Give the extent of all Plasmodium ovale-infected red blood cells.
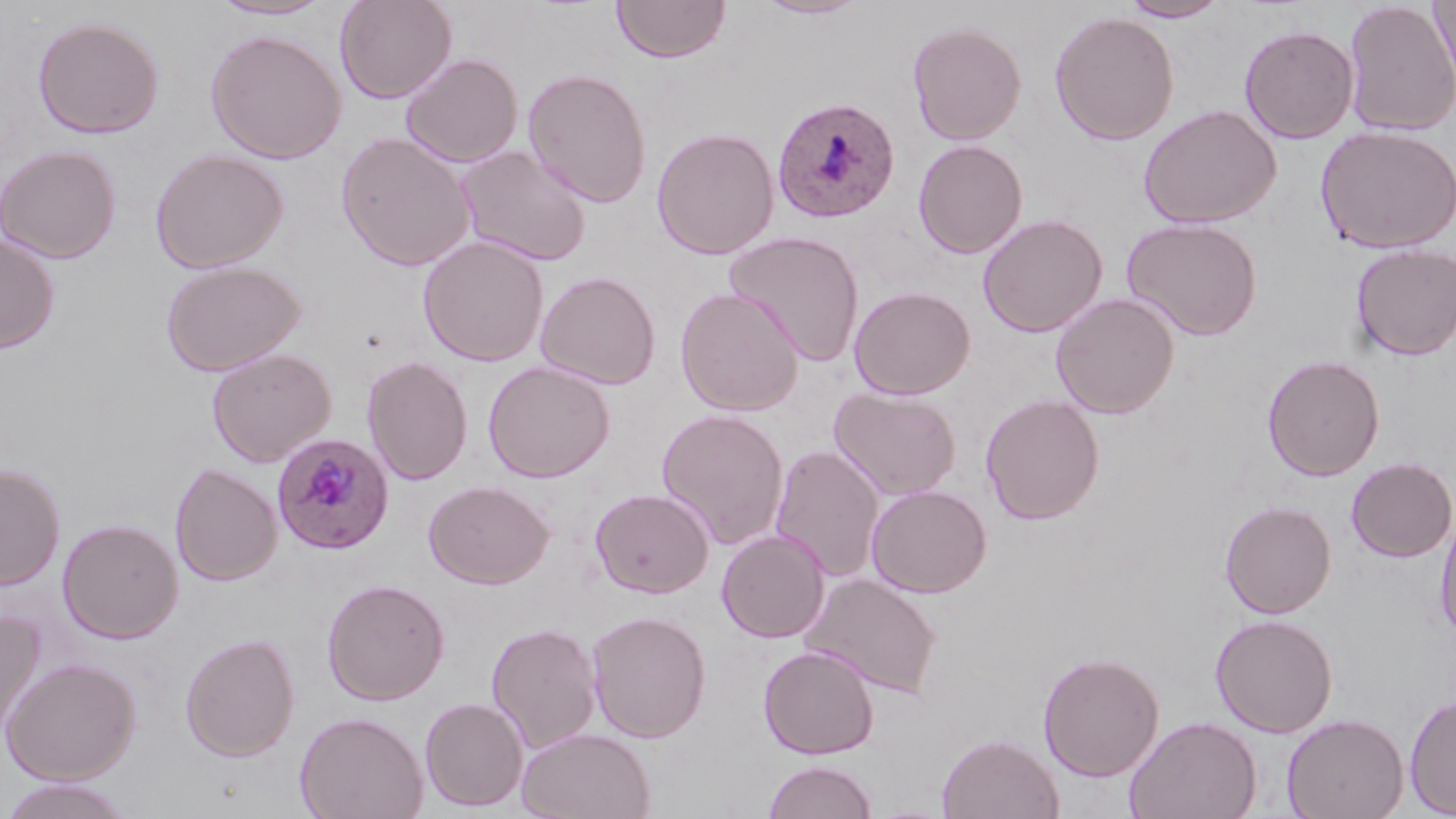

Approximate bounding boxes as named x1/y1/x2/y2 corners in pixels.
Plasmodium ovale-infected red blood cells: (x1=772, y1=95, x2=900, y2=223), (x1=271, y1=433, x2=396, y2=554).

slide-level diagnosis = Plasmodium ovale
uninfected red blood cell locations = approximate bounding boxes as named x1/y1/x2/y2 corners in pixels: (x1=209, y1=0, x2=335, y2=21), (x1=335, y1=0, x2=457, y2=104), (x1=612, y1=0, x2=731, y2=63), (x1=751, y1=0, x2=870, y2=20), (x1=1119, y1=0, x2=1228, y2=22), (x1=1342, y1=0, x2=1456, y2=137), (x1=1428, y1=0, x2=1456, y2=90), (x1=1049, y1=10, x2=1180, y2=145), (x1=32, y1=15, x2=164, y2=139), (x1=907, y1=21, x2=1027, y2=145), (x1=1239, y1=24, x2=1359, y2=143), (x1=205, y1=29, x2=347, y2=165), (x1=400, y1=53, x2=523, y2=168), (x1=523, y1=68, x2=652, y2=208), (x1=1138, y1=104, x2=1281, y2=229), (x1=1315, y1=126, x2=1456, y2=254), (x1=651, y1=127, x2=779, y2=259), (x1=335, y1=132, x2=476, y2=271), (x1=913, y1=139, x2=1028, y2=259), (x1=456, y1=144, x2=592, y2=267), (x1=0, y1=145, x2=121, y2=263), (x1=149, y1=148, x2=288, y2=273), (x1=978, y1=213, x2=1108, y2=337), (x1=1122, y1=217, x2=1263, y2=341), (x1=725, y1=230, x2=865, y2=366), (x1=0, y1=234, x2=60, y2=354), (x1=418, y1=236, x2=549, y2=367), (x1=1350, y1=243, x2=1456, y2=361), (x1=160, y1=258, x2=307, y2=377), (x1=535, y1=271, x2=661, y2=390), (x1=849, y1=285, x2=975, y2=400), (x1=675, y1=286, x2=804, y2=416), (x1=1051, y1=292, x2=1180, y2=418), (x1=207, y1=347, x2=337, y2=467), (x1=1262, y1=354, x2=1385, y2=481), (x1=363, y1=355, x2=473, y2=485), (x1=482, y1=360, x2=616, y2=483), (x1=828, y1=385, x2=961, y2=501), (x1=980, y1=394, x2=1105, y2=525), (x1=656, y1=408, x2=789, y2=549), (x1=770, y1=444, x2=884, y2=582), (x1=1346, y1=457, x2=1456, y2=562), (x1=0, y1=461, x2=66, y2=591), (x1=170, y1=463, x2=282, y2=586), (x1=423, y1=480, x2=554, y2=589), (x1=866, y1=484, x2=992, y2=598), (x1=590, y1=487, x2=714, y2=598), (x1=1220, y1=500, x2=1336, y2=618), (x1=1433, y1=509, x2=1456, y2=641), (x1=57, y1=517, x2=184, y2=644), (x1=717, y1=529, x2=831, y2=643), (x1=801, y1=571, x2=944, y2=700), (x1=321, y1=578, x2=450, y2=705), (x1=0, y1=608, x2=45, y2=743), (x1=586, y1=609, x2=712, y2=744), (x1=1210, y1=614, x2=1338, y2=737), (x1=486, y1=622, x2=602, y2=754), (x1=180, y1=632, x2=300, y2=762), (x1=758, y1=645, x2=879, y2=759), (x1=1038, y1=651, x2=1164, y2=782), (x1=1, y1=657, x2=140, y2=785), (x1=1404, y1=691, x2=1456, y2=817), (x1=420, y1=696, x2=528, y2=811), (x1=294, y1=711, x2=428, y2=819), (x1=1281, y1=713, x2=1408, y2=819), (x1=1125, y1=715, x2=1262, y2=819), (x1=517, y1=727, x2=655, y2=819), (x1=936, y1=732, x2=1065, y2=818), (x1=762, y1=759, x2=879, y2=819), (x1=0, y1=777, x2=134, y2=819)
modality = light microscopy
magnification = 1000x
stain = May-Grünwald-Giemsa
preparation = thin blood film
image size = 1456×819 pixels
field of view = one of a larger specimen